Name the blood parasite species.
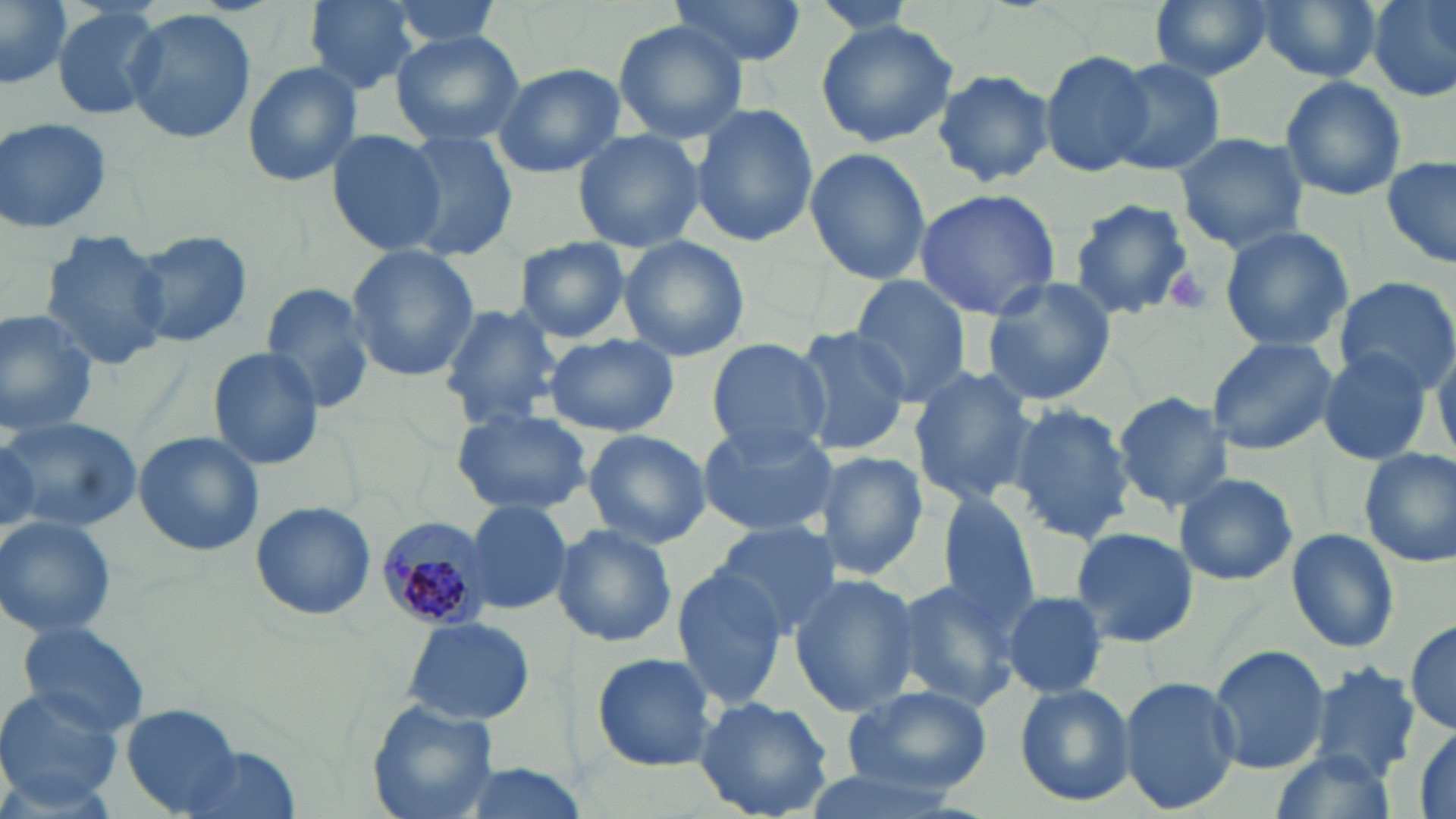
Plasmodium malariae.

Approximate bounding boxes as [x1, y1, x2, y2] in pixels. Platelet locations: [1162, 265, 1212, 315]. Plasmodium malariae-infected red blood cell locations: [374, 513, 493, 634]. Uninfected red blood cell locations: [0, 0, 76, 92], [302, 0, 422, 95], [384, 0, 511, 51], [663, 0, 809, 68], [1148, 0, 1272, 80], [1254, 0, 1382, 84], [1368, 0, 1456, 101], [46, 2, 169, 122], [122, 9, 257, 144], [815, 20, 959, 148], [613, 22, 746, 143], [390, 30, 526, 147], [1039, 48, 1159, 178], [1107, 59, 1229, 177], [239, 60, 363, 187], [491, 62, 625, 179], [932, 70, 1054, 188], [1279, 75, 1406, 202], [689, 102, 819, 250], [0, 116, 116, 236], [574, 127, 702, 255], [327, 130, 445, 255], [1172, 131, 1309, 252], [397, 132, 517, 259], [803, 146, 932, 286], [1382, 155, 1456, 271], [914, 185, 1064, 322], [1068, 200, 1193, 319], [1218, 225, 1354, 352], [126, 230, 254, 349], [37, 231, 170, 372], [619, 236, 749, 362], [513, 237, 632, 343], [346, 246, 480, 380], [847, 273, 975, 407], [979, 275, 1118, 408], [1333, 277, 1455, 392], [260, 279, 377, 411], [436, 300, 565, 428], [0, 307, 102, 434], [792, 324, 915, 456], [544, 333, 679, 437], [1206, 335, 1337, 457], [705, 336, 832, 456], [1433, 337, 1456, 459], [206, 346, 326, 470], [1316, 350, 1433, 465], [907, 365, 1037, 506], [1113, 391, 1234, 510], [1009, 403, 1136, 544], [451, 407, 592, 516], [2, 414, 143, 532], [695, 418, 838, 537], [583, 429, 711, 547], [132, 430, 263, 557], [0, 433, 44, 541], [0, 436, 43, 532], [814, 449, 931, 582], [1358, 449, 1455, 568], [1171, 472, 1300, 586], [933, 489, 1044, 627], [463, 498, 572, 615], [250, 500, 376, 621], [0, 516, 119, 640], [712, 520, 840, 640], [550, 524, 677, 647], [1068, 527, 1198, 648], [1285, 528, 1399, 653], [671, 563, 790, 709], [789, 572, 920, 719], [891, 579, 1022, 710], [1003, 591, 1109, 699], [402, 615, 535, 726], [15, 618, 152, 737], [1405, 619, 1456, 733], [1206, 643, 1330, 775], [590, 651, 722, 773], [1307, 662, 1422, 782], [1121, 677, 1241, 813], [1014, 684, 1137, 807], [0, 686, 120, 808], [842, 686, 991, 796], [693, 697, 835, 819], [367, 701, 499, 819], [121, 705, 244, 816], [1410, 722, 1455, 819], [173, 745, 301, 819], [1266, 750, 1401, 819], [443, 763, 596, 819], [790, 766, 966, 818]. One field of a larger specimen. 1000x magnification. Image is 1456×819 pixels. May-Grünwald-Giemsa-stained preparation. Thin blood film. Optical microscopy.